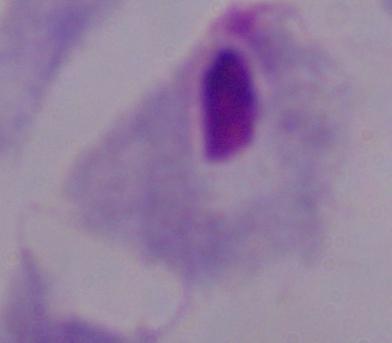
Micrograph. A trichomonad is seen. Captured at 1000x magnification.